Name the blood parasite species.
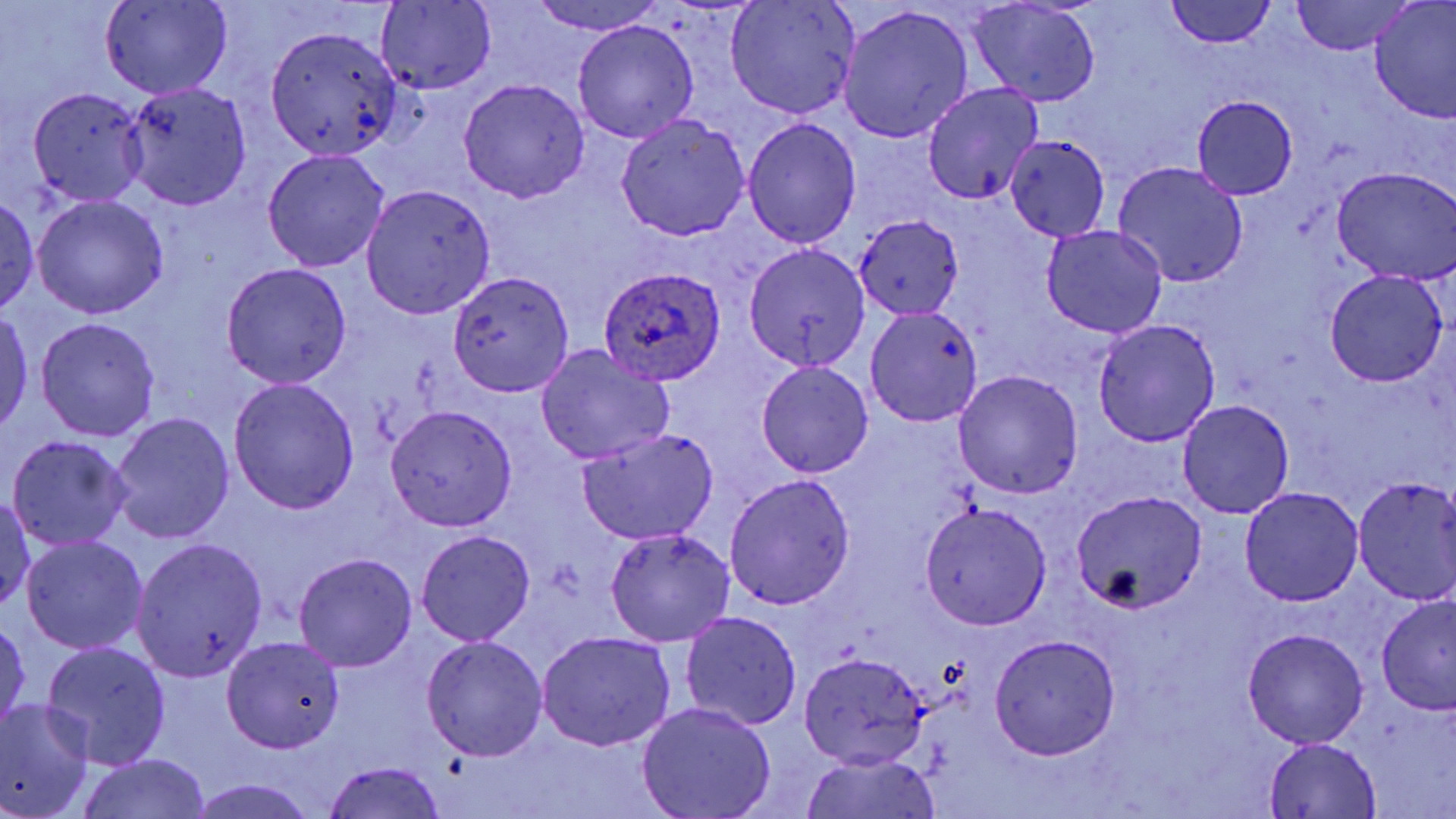

Plasmodium ovale.

Approximate bounding boxes as [x1, y1, x2, y2] in pixels. Plasmodium ovale-infected red blood cell locations: [598, 267, 727, 385]. Uninfected red blood cell locations: [725, 0, 860, 120], [1165, 0, 1275, 50], [1369, 0, 1456, 121], [376, 1, 496, 94], [529, 1, 666, 36], [1289, 1, 1412, 53], [100, 2, 232, 99], [968, 2, 1101, 106], [838, 6, 974, 144], [572, 20, 698, 143], [266, 25, 403, 162], [456, 78, 590, 202], [122, 80, 252, 210], [922, 83, 1044, 204], [28, 87, 149, 206], [1192, 96, 1299, 199], [616, 115, 750, 241], [743, 116, 862, 246], [1005, 134, 1111, 241], [263, 149, 388, 272], [1112, 161, 1249, 288], [1331, 167, 1456, 285], [361, 184, 497, 319], [1, 193, 41, 316], [32, 195, 168, 319], [853, 216, 964, 317], [1040, 224, 1169, 338], [744, 242, 870, 374], [222, 263, 352, 387], [448, 267, 575, 398], [1324, 270, 1448, 387], [865, 306, 984, 428], [1, 310, 34, 437], [36, 317, 161, 441], [1092, 319, 1222, 446], [534, 345, 675, 465], [754, 360, 874, 478], [953, 369, 1084, 500], [228, 378, 360, 514], [1176, 399, 1295, 519], [384, 405, 517, 531], [108, 412, 235, 545], [578, 430, 719, 544], [7, 434, 133, 550], [724, 473, 856, 609], [1352, 477, 1456, 604], [1240, 486, 1363, 607], [1070, 490, 1206, 614], [0, 492, 36, 612], [919, 501, 1052, 629], [604, 527, 736, 647], [415, 529, 536, 647], [20, 536, 149, 655], [133, 536, 267, 679], [292, 553, 418, 672], [1374, 595, 1456, 715], [678, 611, 802, 731], [1, 617, 30, 735], [1241, 628, 1368, 748], [536, 631, 676, 752], [990, 631, 1120, 759], [220, 635, 346, 755], [420, 635, 548, 761], [41, 640, 173, 768], [798, 652, 932, 770], [0, 700, 95, 819], [636, 702, 777, 819], [1263, 737, 1382, 818], [798, 751, 946, 819], [78, 754, 212, 819], [321, 760, 449, 819], [192, 777, 316, 819]. Light microscopy. Single field of view. Thin blood smear. Image is 1456×819 pixels. May-Grünwald-Giemsa stain. Captured at 1000x magnification.